Assess the background quality.
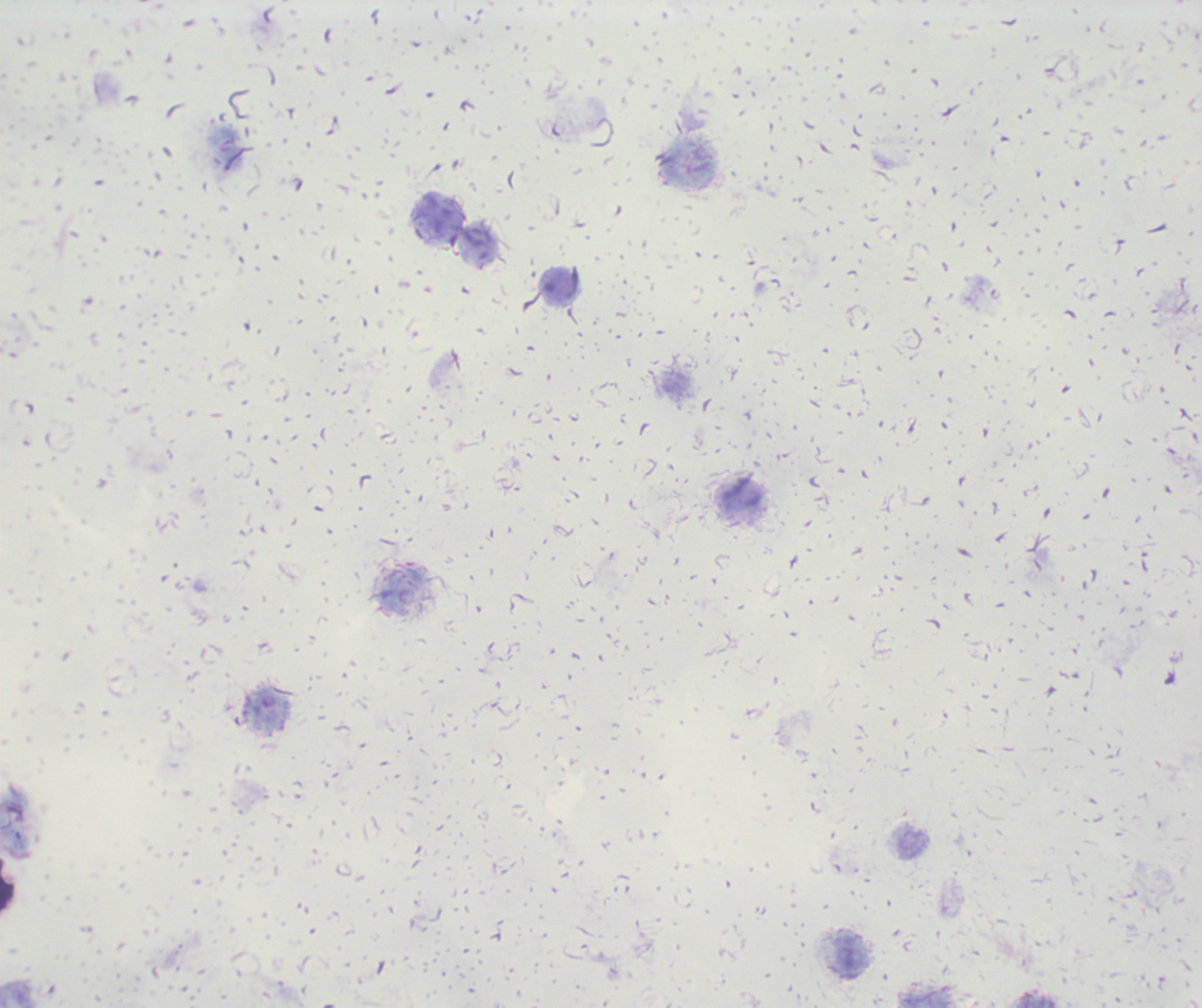
Poor.

coordinate format = approximate centers as {x, y} in pixels
leukocyte locations = {690, 166}, {441, 215}, {560, 287}, {741, 495}, {402, 589}, {851, 953}
preparation = thick smear of blood
context = previously used in an actual diagnosis
magnification = 100x
image size = 1202×1008 pixels
stain = Romanowsky
result = no malaria parasites seen
field of view = one from this slide